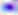
{
  "identification": "Toxoplasma gondii",
  "magnification": "400x",
  "modality": "photomicrograph"
}